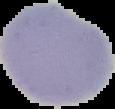

Summary:
  - Image size: 115×109 pixels
  - Preparation: thin blood film
  - Image type: segmented cell region on a black background
  - Result: no malaria parasites seen